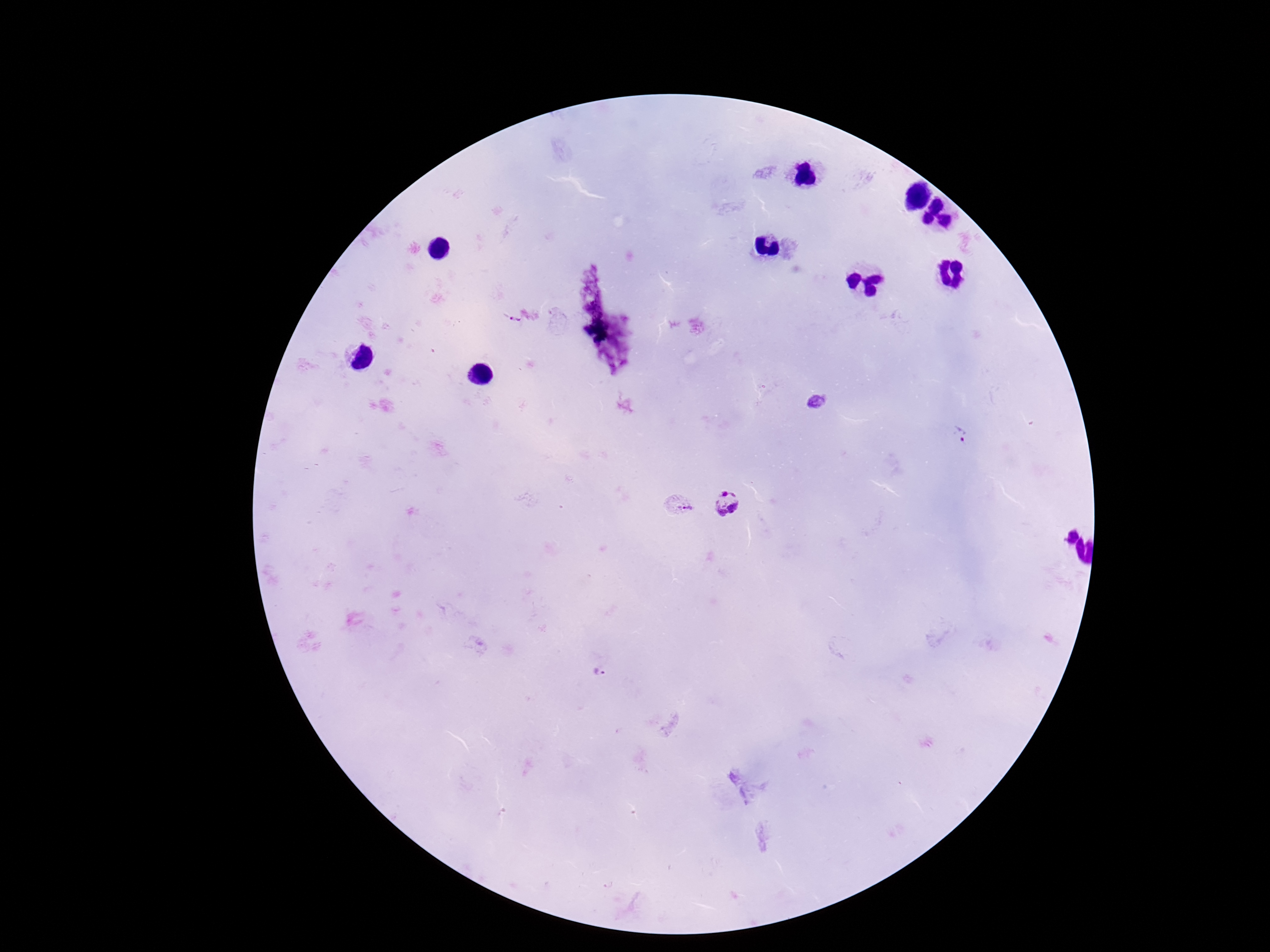
Approximate centers as (x, y) in pixels. Plasmodium parasite locations: (514, 317), (817, 401), (961, 435), (727, 501), (677, 506), (601, 672). Thick peripheral-blood smear. Image is 1270×952 pixels. Photographed through the microscope eyepiece with a smartphone camera. Patient malaria status: positive. 100x magnification. Single field of view. Giemsa-stained preparation.